Assess the morphology of the red blood cells.
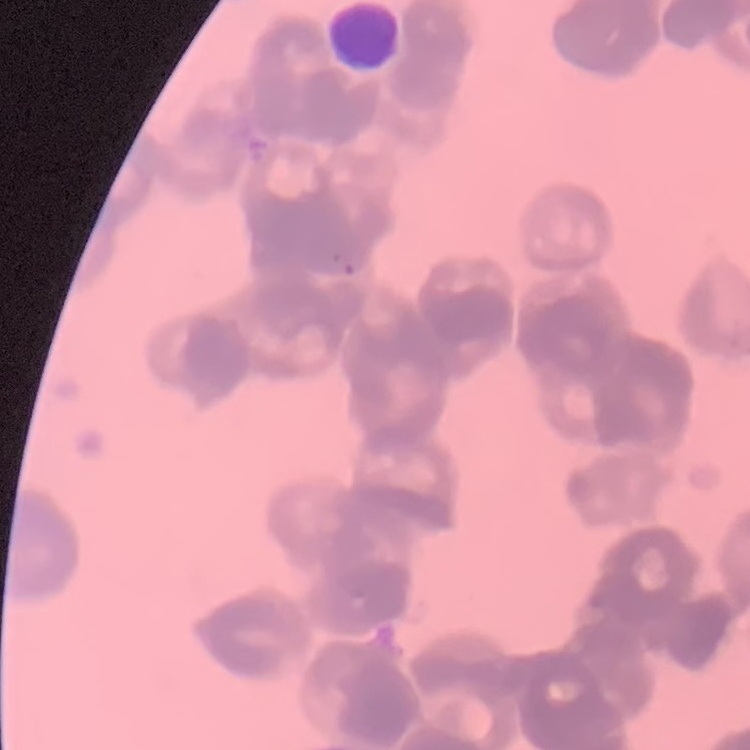
They show rouleaux formation.

Square crop of a larger photomicrograph. Stained with either Field's or Giemsa. Thin blood film.